Name the parasite shown.
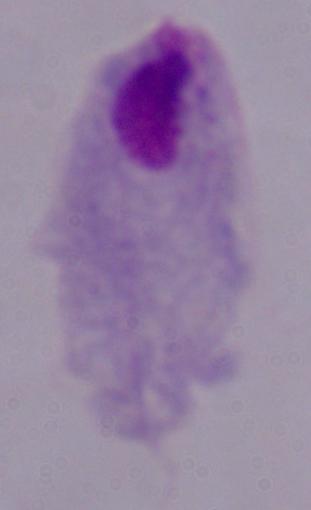
A trichomonad.

modality = photomicrograph
magnification = 1000x